Assess this cell for malaria.
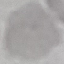
Uninfected.

Summary:
  - Image type: automatically extracted cell patch, resized to 64 × 64 pixels
  - Capture: smartphone through the microscope eyepiece
  - Preparation: thin smear
  - Stain: Giemsa